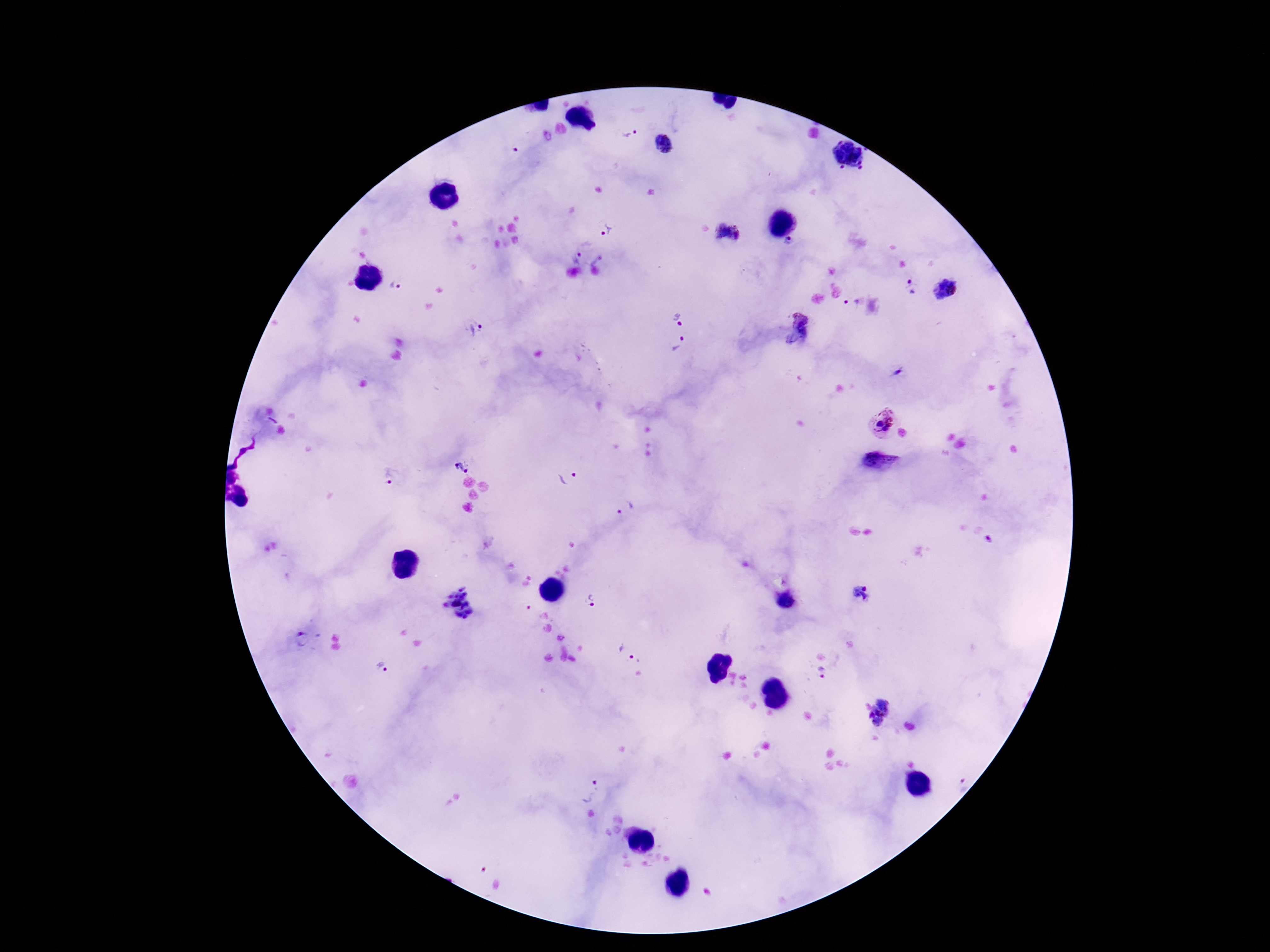
Approximate centers as {x, y} in pixels.
Summary:
  - Plasmodium parasite locations: {630, 133}, {665, 144}, {847, 157}, {606, 230}, {728, 232}, {790, 241}, {579, 257}, {598, 258}, {395, 286}, {912, 286}, {946, 289}, {850, 303}, {679, 317}, {797, 326}, {474, 327}, {680, 346}, {898, 373}, {883, 422}, {879, 462}, {461, 466}, {392, 477}, {567, 478}, {626, 508}, {990, 539}, {861, 593}, {591, 601}, {786, 601}, {463, 605}, {302, 640}, {627, 652}, {382, 668}, {824, 672}, {885, 714}, {958, 781}, {591, 791}
  - Capture: smartphone camera through the microscope eyepiece
  - Patient malaria status: infected
  - Stain: Giemsa
  - Magnification: 100x
  - Image size: 1270×952 pixels
  - Field of view: single
  - Preparation: thick peripheral-blood smear